Assess this cell for malaria.
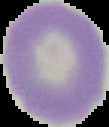

Uninfected.

Image is 109×127 pixels. From a thin blood film. The area outside the segmented cell region is set to black.